State which parasite is depicted.
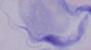

This is a trypanosome.

1000x magnification. Photomicrograph.